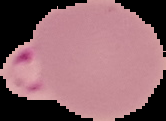
image type = segmented cell region with the area outside set to black
image size = 166×121 pixels
result = malaria parasites identified
preparation = thin blood smear